Name the parasite shown.
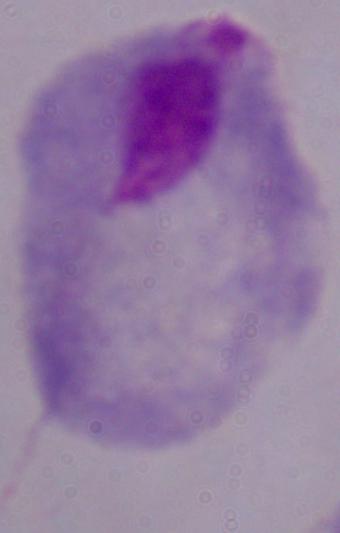
This is a trichomonad.

modality = photomicrograph
magnification = 1000x